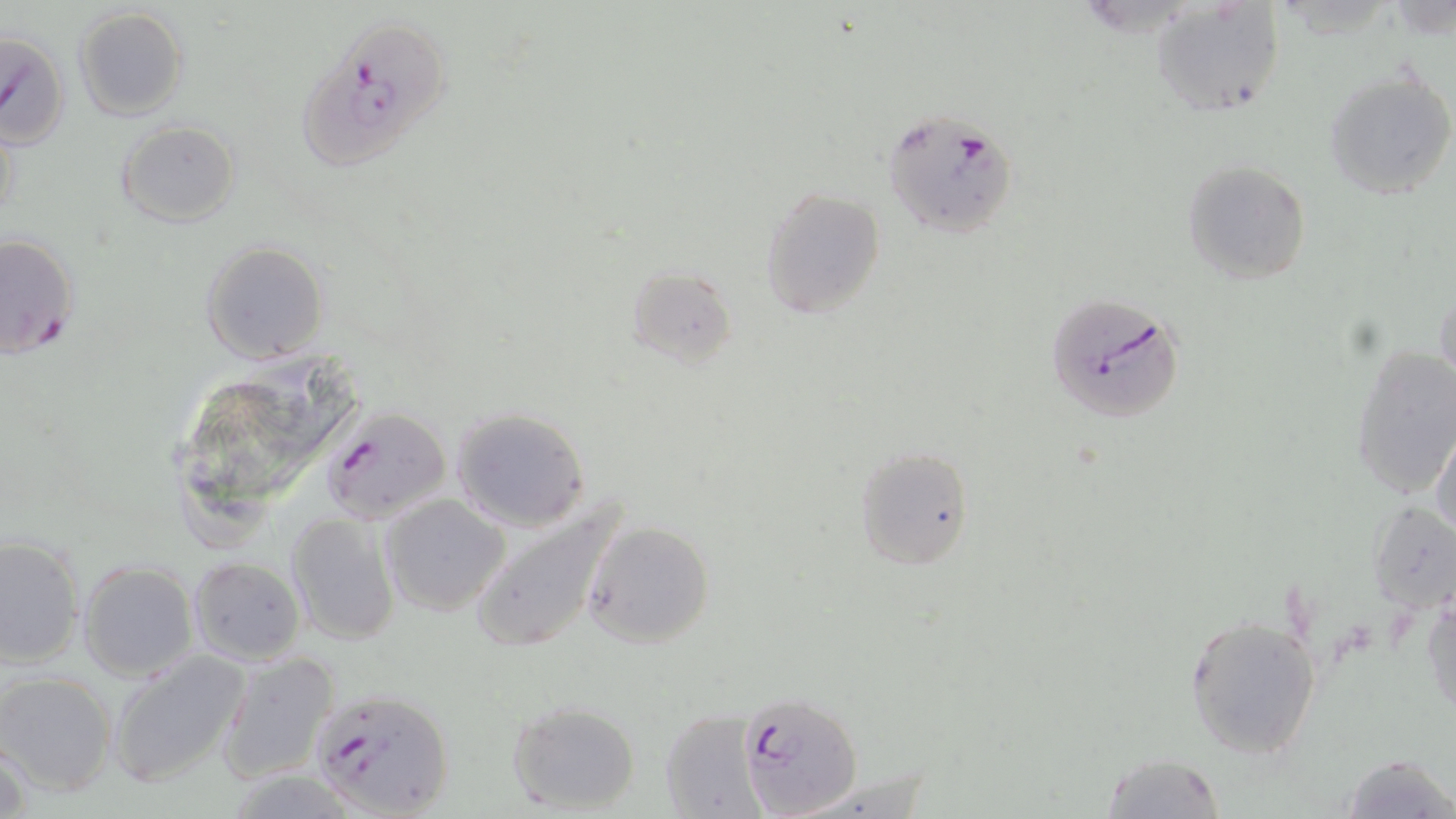
Summary:
  - Coordinate format: approximate bounding boxes as (x1, y1, x2, y2) in pixels
  - Plasmodium falciparum-infected red blood cell locations: (295, 24, 446, 178), (0, 31, 70, 150), (883, 112, 1018, 238), (0, 232, 79, 360), (1046, 293, 1185, 425), (321, 408, 453, 524), (308, 685, 455, 818), (735, 697, 866, 818)
  - Uninfected red blood cell locations: (1150, 1, 1283, 115), (73, 7, 189, 122), (1323, 68, 1456, 201), (1, 112, 19, 232), (115, 120, 239, 227), (1182, 161, 1310, 282), (761, 187, 886, 321), (200, 241, 329, 365), (622, 266, 737, 370), (1434, 287, 1455, 394), (1350, 345, 1455, 500), (451, 407, 590, 532), (1430, 421, 1456, 540), (853, 445, 974, 570), (381, 493, 512, 616), (468, 495, 628, 657), (1370, 501, 1456, 616), (285, 512, 400, 646), (581, 520, 715, 649), (0, 535, 84, 669), (189, 556, 305, 664), (77, 559, 198, 680), (1422, 584, 1455, 718), (1185, 613, 1321, 759), (107, 650, 251, 791), (216, 650, 342, 784), (1, 671, 119, 796), (505, 701, 640, 815), (660, 709, 764, 817), (0, 734, 36, 819), (1100, 753, 1226, 818), (1338, 754, 1455, 819), (797, 771, 935, 819)
  - Slide-level diagnosis: Plasmodium falciparum
  - Magnification: 1000x
  - Stain: May-Grünwald-Giemsa
  - Preparation: thin blood film
  - Image size: 1456×819 pixels
  - Field of view: single
  - Modality: light microscopy